Give the position of every Plasmodium parasite.
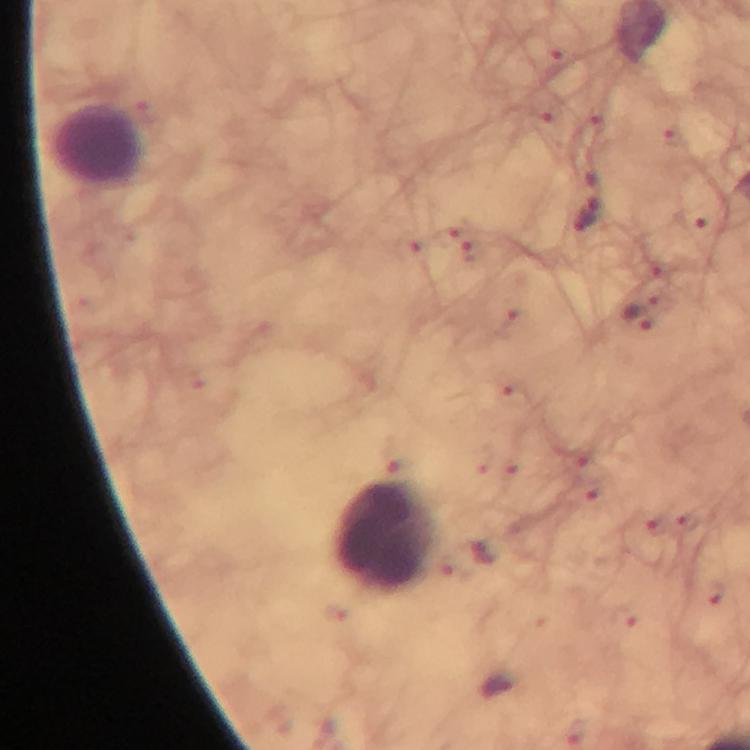

Approximate centers as [x, y] in pixels.
Plasmodium parasites: [674, 139], [593, 186], [691, 219], [582, 222], [635, 317].

Summary:
  - Leukocyte locations: [100, 145], [384, 531]
  - Preparation: thick blood film
  - Image size: 750×750 pixels
  - Immersion oil: used
  - Cropped from: a single field of view
  - Stain: Giemsa
  - Capture: smartphone camera through the microscope
  - Magnification: 100x
  - Context: from a diagnostic examination for malaria